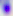
Summary:
  - Identification: Toxoplasma gondii
  - Modality: micrograph
  - Magnification: 400x